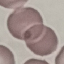

malaria status = uninfected
image type = cell patch, automatically extracted from a larger field of view and resized to 64 × 64 pixels
stain = Giemsa
capture = smartphone through the microscope eyepiece
preparation = thin blood smear